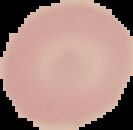
Result: no Plasmodium parasites detected. Image is 133×130 pixels. From a thin blood film. Cell region segmented out of the field of view; the surrounding area is masked to black.